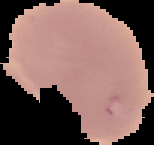

image_size: 154×145 pixels
image_type: segmented cell region on a black background
preparation: thin blood smear
result: no Plasmodium parasites detected